Describe the morphology of the erythrocytes.
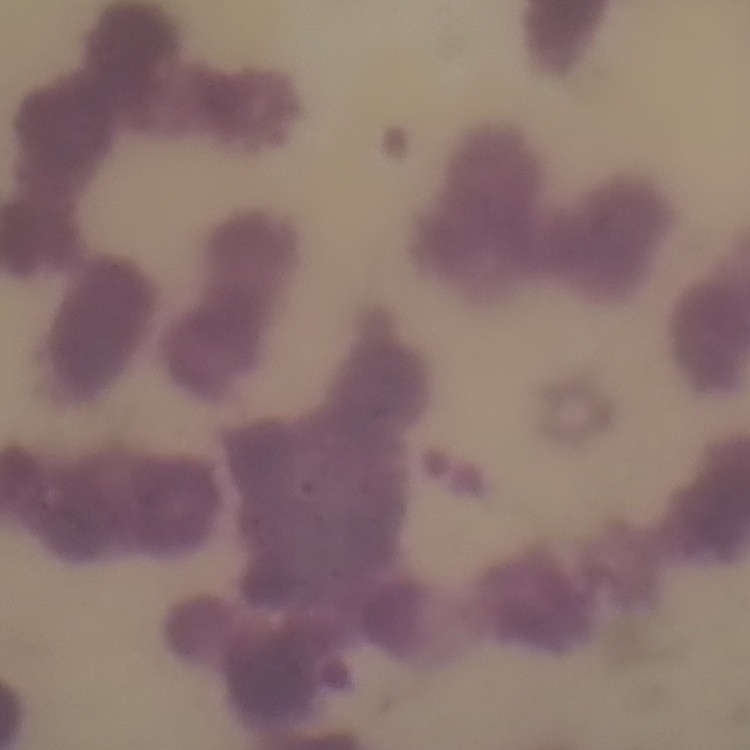

Rouleaux formation.

{
  "preparation": "thin peripheral smear",
  "image_type": "one tile cut from a larger photomicrograph",
  "stain": "Field's or Giemsa"
}